Point out each Plasmodium parasite.
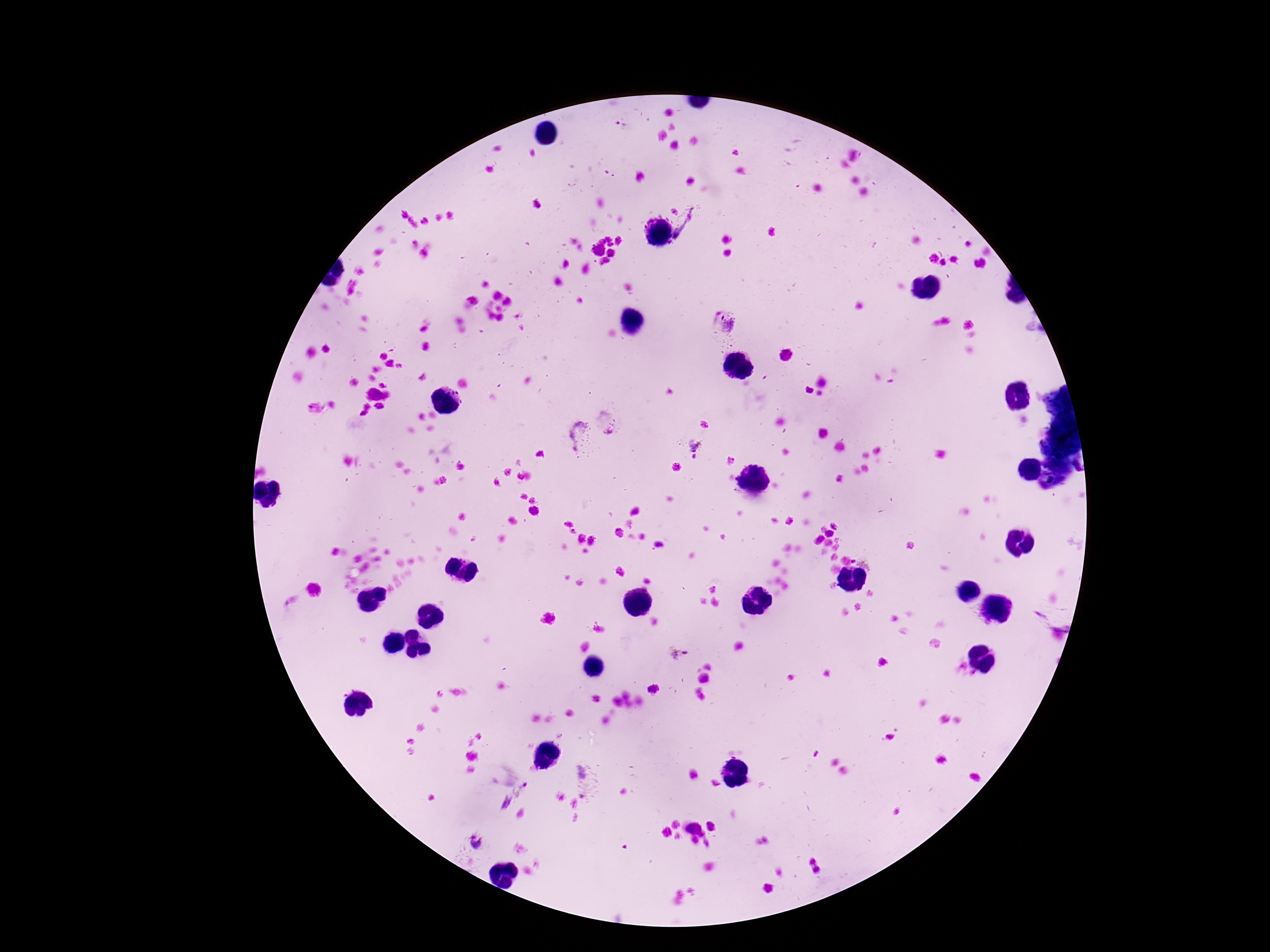

Approximate centers as [x, y] in pixels.
Plasmodium parasites: [689, 225], [722, 324], [609, 420], [578, 436], [694, 443], [679, 655], [654, 689], [587, 780], [474, 842].

Summary:
  - Capture: smartphone camera through the microscope eyepiece
  - Preparation: thick blood film
  - Patient malaria status: infected
  - Image size: 1270×952 pixels
  - Field of view: single
  - Stain: Giemsa
  - Magnification: 100x